Identify the cell.
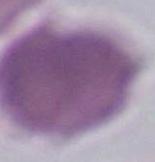

This is an erythrocyte.

Micrograph. Captured at 1000x magnification.